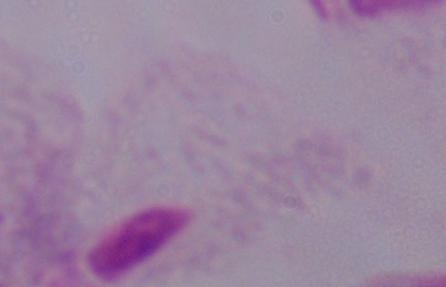
Summary:
  - Modality: micrograph
  - Magnification: 1000x
  - Identification: trichomonad